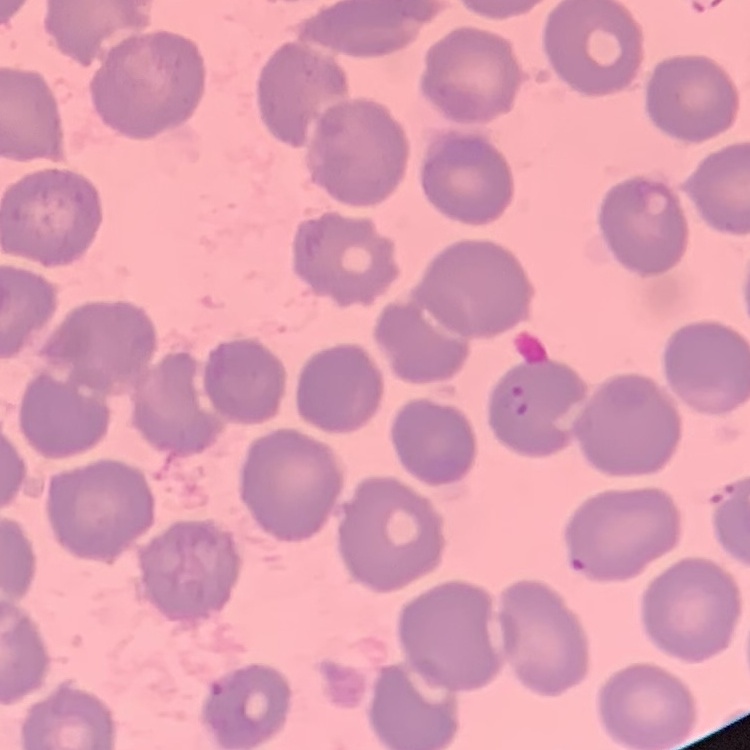
The red blood cells exhibit no rouleaux formation. Square crop of a larger photomicrograph. Stained with either Field's or Giemsa. Thin blood film.